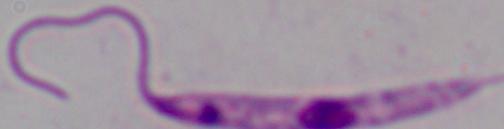
1000x magnification. Micrograph. A Leishmania parasite is seen.